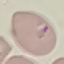
Summary:
  - Result: malaria parasites detected
  - Preparation: thin smear
  - Image type: automatically extracted cell patch, resized to 64 × 64 pixels
  - Stain: Giemsa
  - Capture: smartphone through the microscope eyepiece